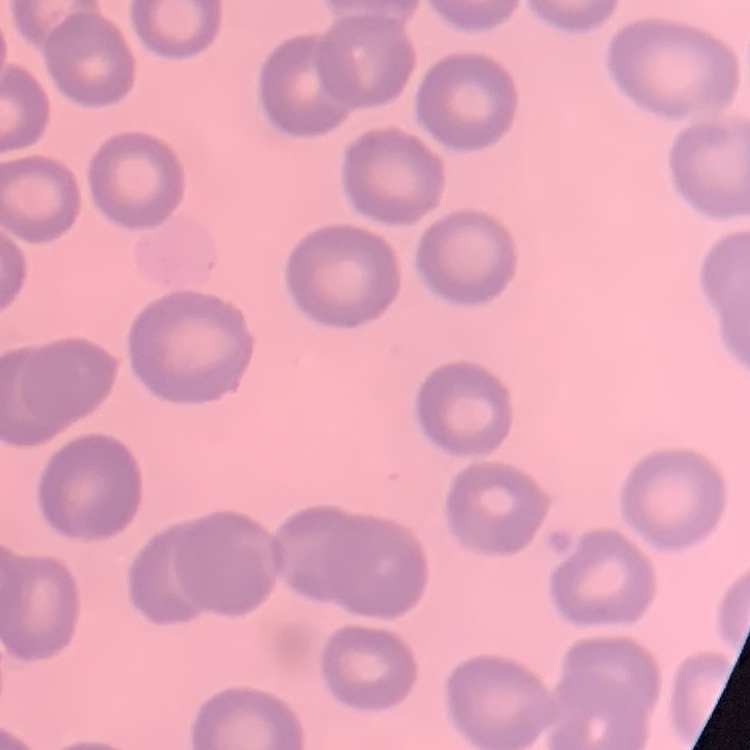

erythrocyte morphology = no rouleaux formation
image type = square crop of a larger photomicrograph
preparation = thin blood film
stain = Field's or Giemsa